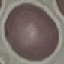

Malaria status: uninfected. Automatically extracted cell patch, resized to 64 × 64 pixels. Acquired by smartphone through the microscope eyepiece. Thin smear of blood. Giemsa-stained preparation.